State the preparation type.
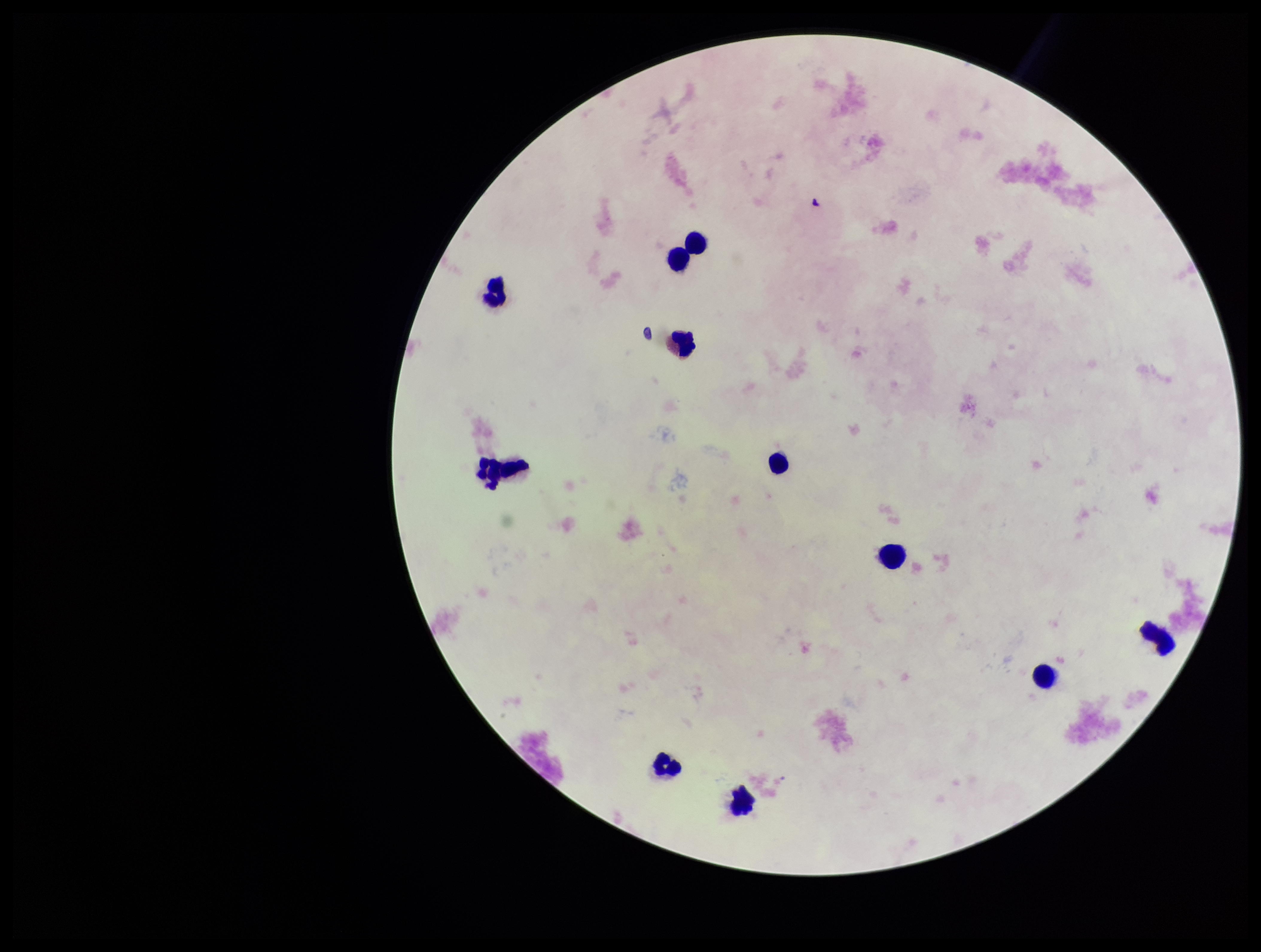

A thick smear.

Summary:
  - Field of view: one from this slide
  - Stain: Giemsa
  - Patient malaria status: negative
  - Plasmodium parasites: none detected
  - Image size: 1261×952 pixels
  - Leukocyte count: 11
  - Parasite count: 0
  - Capture: smartphone photograph through the microscope eyepiece